Locate every P. falciparum parasite and identify its life-cycle stage.
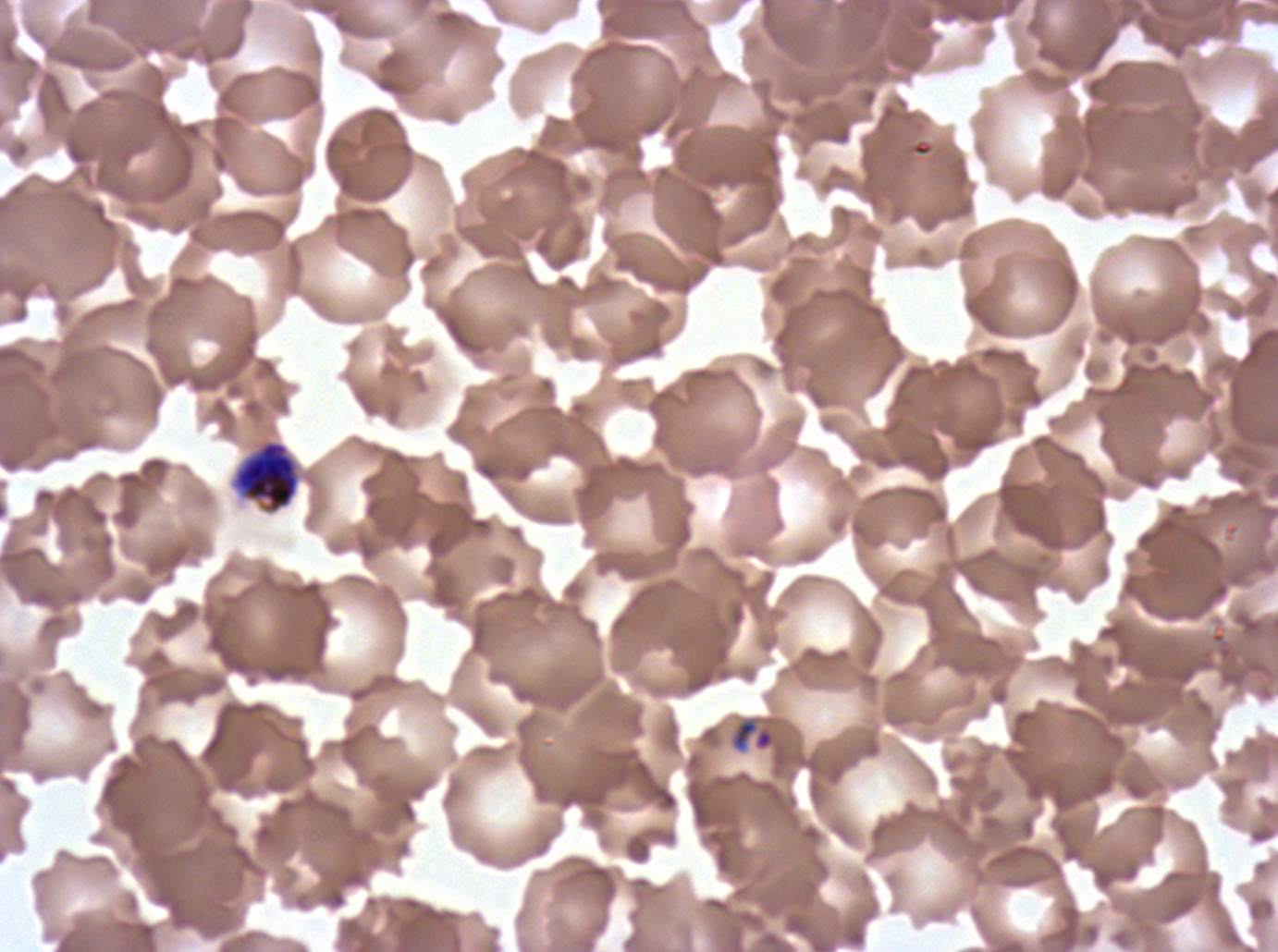

Approximate bounding rectangles given as corner coordinates in pixels from the top-left.
Rings: (x1=731, y1=718, x2=775, y2=751).
No late-ring/early-trophozoite forms, mid trophozoites, late trophozoites, early schizonts, late schizonts, segmenters, or gametocytes observed.

Summary:
  - Preparation: thin blood smear
  - Field of view: sub-image separated from a larger composite
  - Image size: 1278×952 pixels
  - Stain: Giemsa
  - Specimen: P. falciparum cultured ex vivo for 24 to 48 hours, from a patient in The Gambia